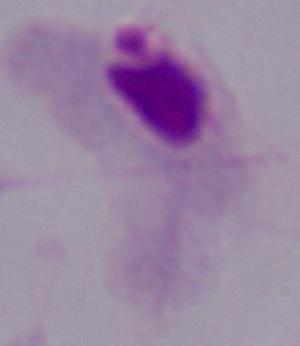
Captured at 1000x magnification. Photomicrograph. A trichomonad is shown.